Assess for Plasmodium parasites.
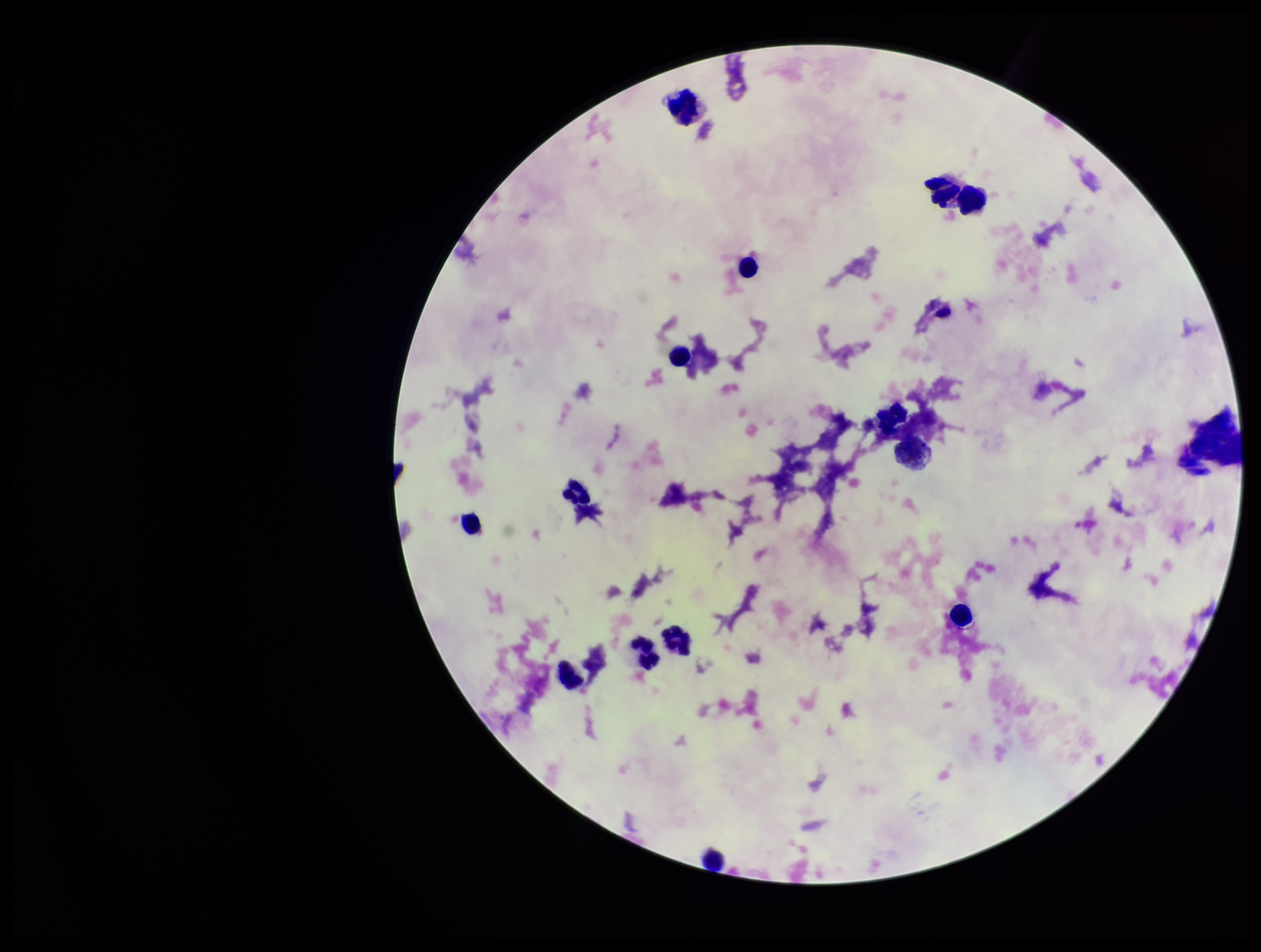
None detected.

leukocyte count = 14
capture = smartphone photograph through the microscope eyepiece
image size = 1261×952 pixels
parasite count = 0
stain = Giemsa
patient malaria status = negative
preparation = thick smear
field of view = one from this slide